Classify this cell by malaria status.
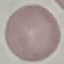
It is uninfected.

Thin smear of blood. Giemsa stain. Automatically extracted cell patch, resized to 64 × 64 pixels. Photographed with a smartphone camera at the microscope eyepiece.